Classify this cell by malaria status.
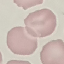
It is uninfected.

Summary:
  - Image type: automatically extracted cell patch, resized to 64 × 64 pixels
  - Capture: smartphone camera at the microscope eyepiece
  - Preparation: thin blood smear
  - Stain: Giemsa